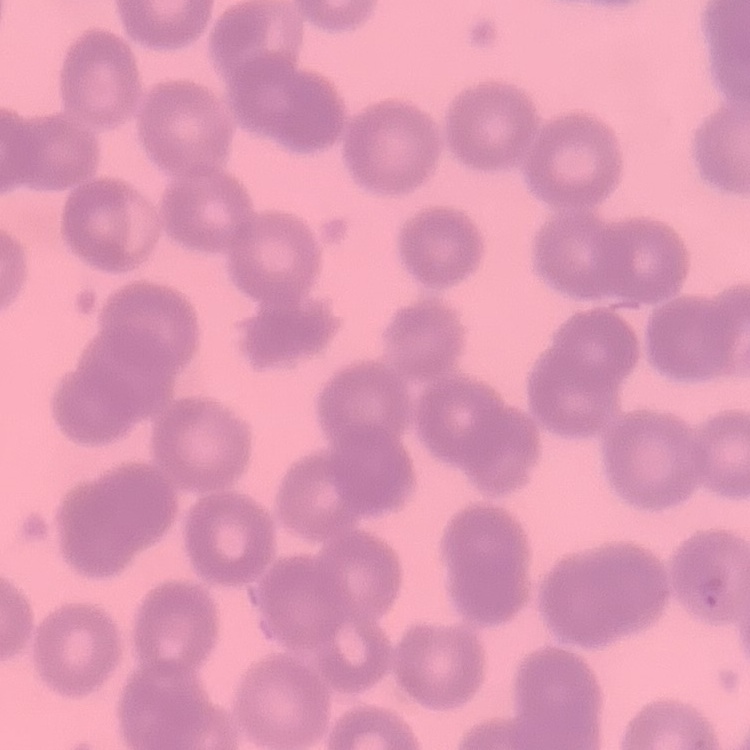

The erythrocytes show no rouleaux formation. Thin peripheral smear. Field's or Giemsa stain. One tile cut from a larger photomicrograph.